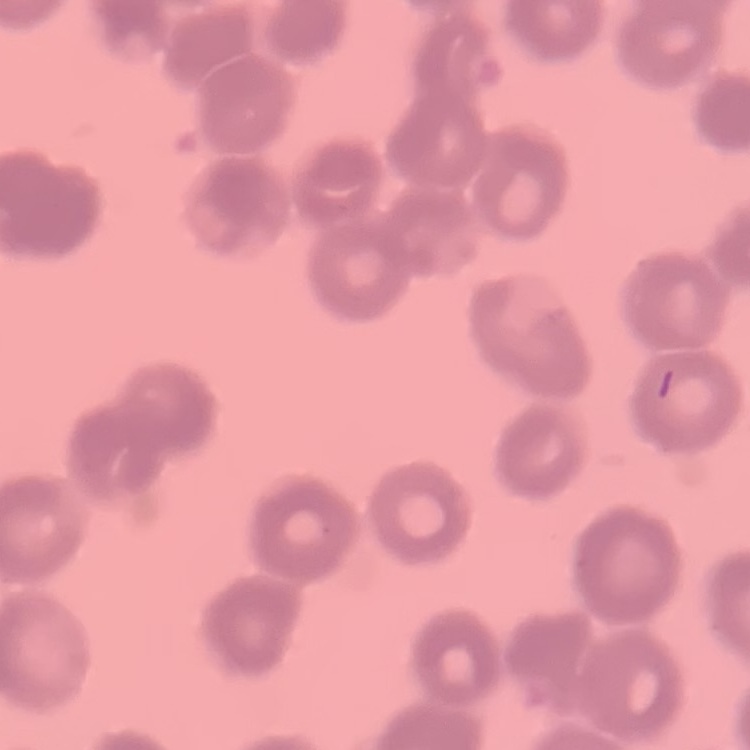
erythrocyte_morphology: rouleaux formation
preparation: thin blood film
stain: Field's or Giemsa
image_type: one tile cut from a larger photomicrograph